Assess the morphology of the red blood cells.
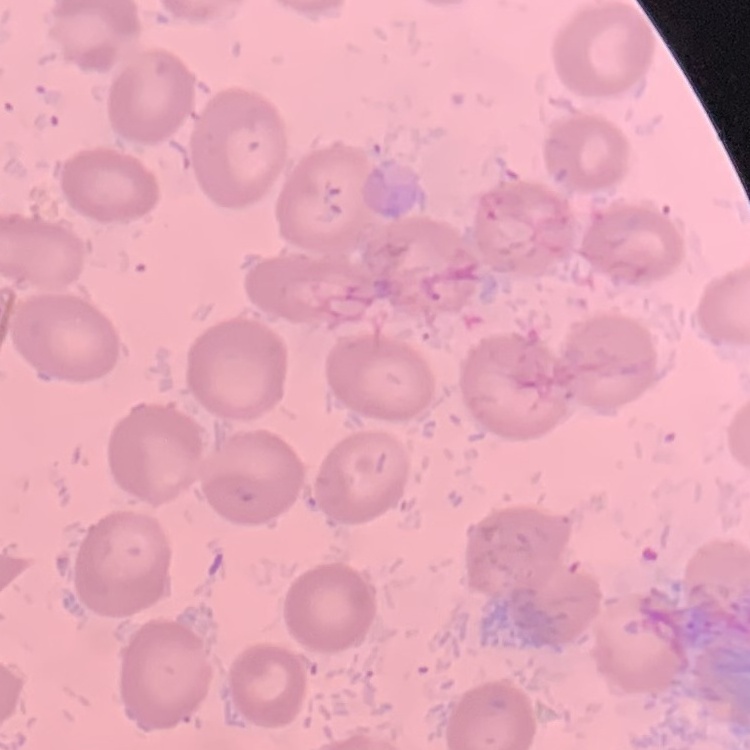

They show no rouleaux formation.

Square crop of a larger photomicrograph. Thin peripheral smear. Field's or Giemsa stain.